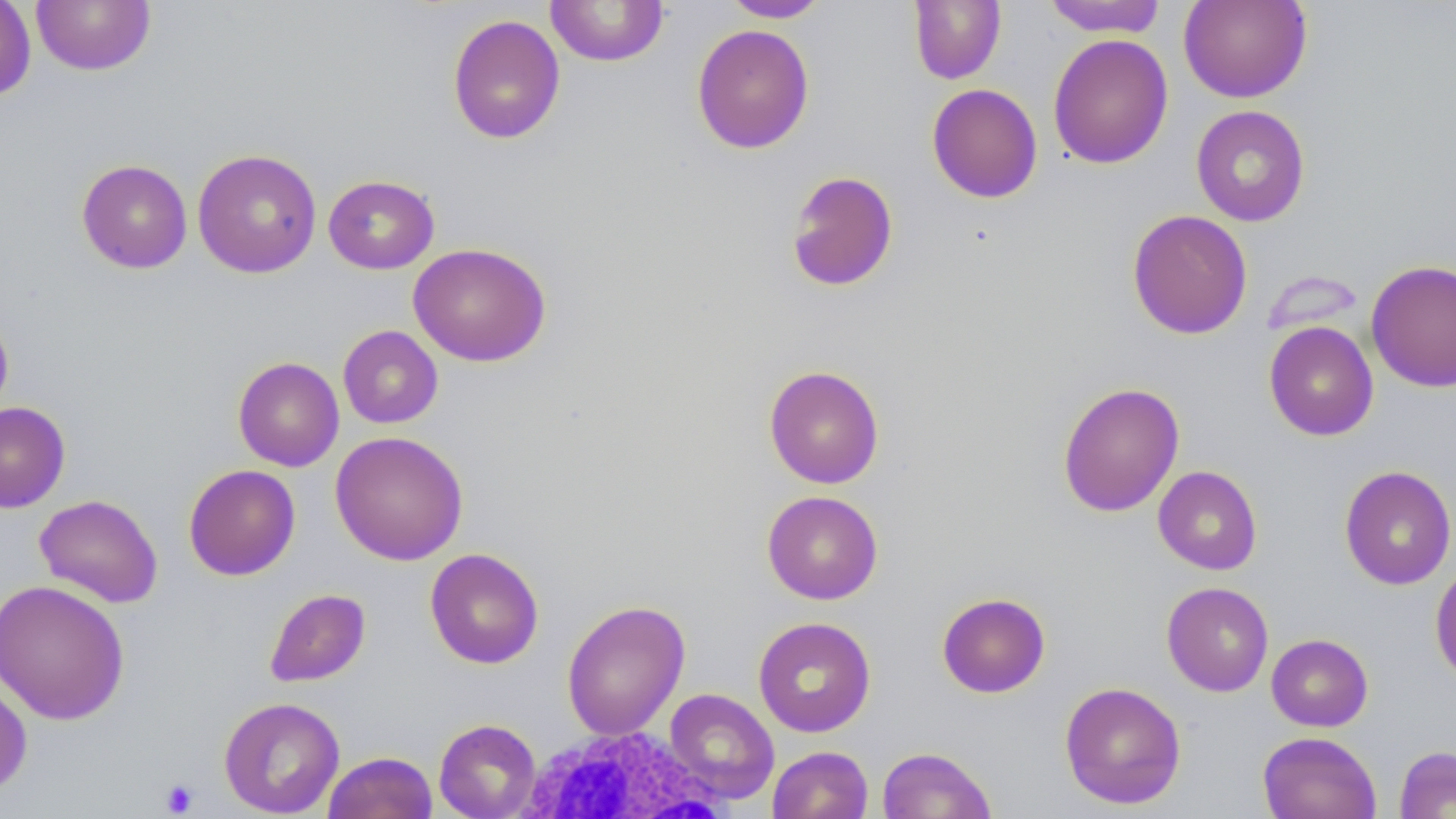

Summary:
  - Coordinate format: approximate bounding boxes as named x1/y1/x2/y2 corners in pixels
  - White blood cell locations: (x1=517, y1=725, x2=734, y2=817)
  - Platelet locations: (x1=159, y1=778, x2=199, y2=816)
  - Uninfected red blood cell locations: (x1=0, y1=0, x2=36, y2=102), (x1=720, y1=0, x2=831, y2=22), (x1=908, y1=0, x2=1006, y2=84), (x1=1042, y1=0, x2=1168, y2=37), (x1=1178, y1=0, x2=1312, y2=103), (x1=31, y1=1, x2=156, y2=75), (x1=544, y1=1, x2=670, y2=67), (x1=446, y1=14, x2=566, y2=145), (x1=691, y1=23, x2=815, y2=154), (x1=1047, y1=34, x2=1173, y2=169), (x1=926, y1=83, x2=1043, y2=204), (x1=1190, y1=105, x2=1311, y2=226), (x1=192, y1=148, x2=322, y2=278), (x1=76, y1=159, x2=193, y2=273), (x1=784, y1=170, x2=899, y2=293), (x1=322, y1=174, x2=439, y2=274), (x1=1126, y1=209, x2=1253, y2=340), (x1=408, y1=242, x2=551, y2=367), (x1=1366, y1=259, x2=1456, y2=392), (x1=0, y1=309, x2=14, y2=423), (x1=1263, y1=321, x2=1379, y2=441), (x1=338, y1=325, x2=443, y2=429), (x1=233, y1=356, x2=344, y2=471), (x1=763, y1=364, x2=885, y2=489), (x1=1057, y1=381, x2=1185, y2=517), (x1=0, y1=401, x2=71, y2=512), (x1=330, y1=430, x2=469, y2=565), (x1=183, y1=464, x2=300, y2=581), (x1=1152, y1=465, x2=1263, y2=575), (x1=1339, y1=465, x2=1456, y2=590), (x1=762, y1=490, x2=884, y2=605), (x1=34, y1=494, x2=163, y2=608), (x1=424, y1=548, x2=544, y2=669), (x1=1430, y1=560, x2=1456, y2=685), (x1=0, y1=579, x2=130, y2=726), (x1=1161, y1=582, x2=1274, y2=697), (x1=263, y1=588, x2=371, y2=687), (x1=936, y1=592, x2=1051, y2=698), (x1=561, y1=599, x2=690, y2=741), (x1=752, y1=616, x2=876, y2=737), (x1=1266, y1=633, x2=1373, y2=731), (x1=0, y1=673, x2=33, y2=798), (x1=1059, y1=681, x2=1187, y2=809), (x1=664, y1=688, x2=779, y2=804), (x1=218, y1=697, x2=345, y2=817), (x1=433, y1=718, x2=542, y2=819), (x1=1257, y1=731, x2=1382, y2=819), (x1=1394, y1=745, x2=1456, y2=818), (x1=767, y1=746, x2=873, y2=819), (x1=877, y1=746, x2=997, y2=819), (x1=322, y1=751, x2=438, y2=819)
  - Slide-level diagnosis: no evidence of blood parasites
  - Magnification: 1000x
  - Image size: 1456×819 pixels
  - Field of view: single
  - Stain: May-Grünwald-Giemsa
  - Preparation: thin blood film
  - Modality: light microscopy